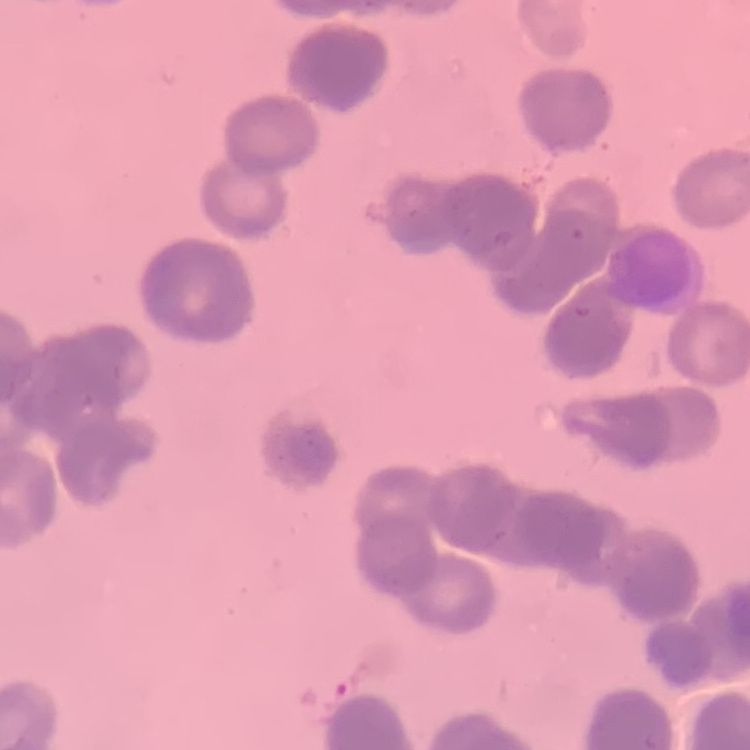 The erythrocytes exhibit rouleaux formation. One tile cut from a larger photomicrograph. Stained with either Field's or Giemsa. Thin blood smear.